Comment on the morphology of the erythrocytes.
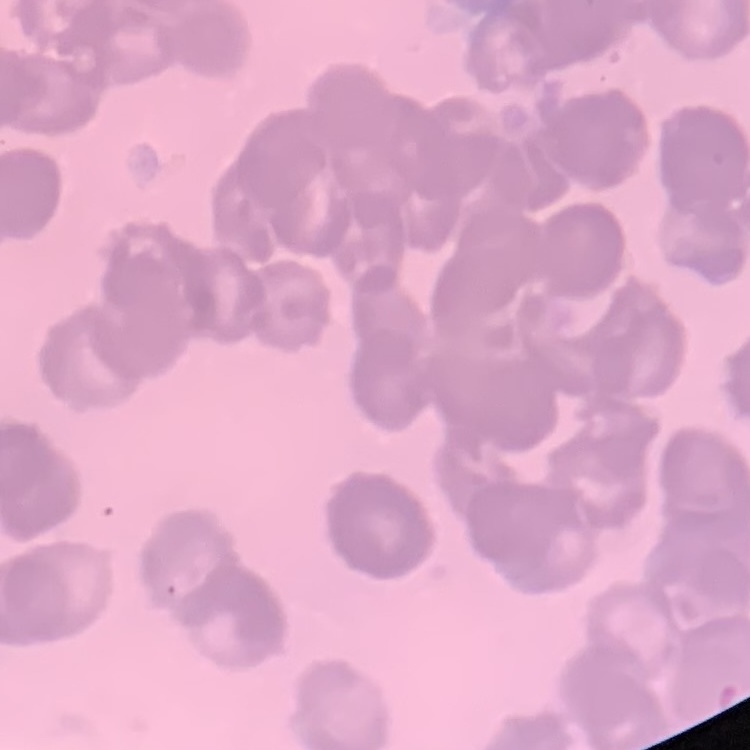
Rouleaux formation.

Summary:
  - Image type: square crop of a larger photomicrograph
  - Preparation: thin blood smear
  - Stain: Field's or Giemsa